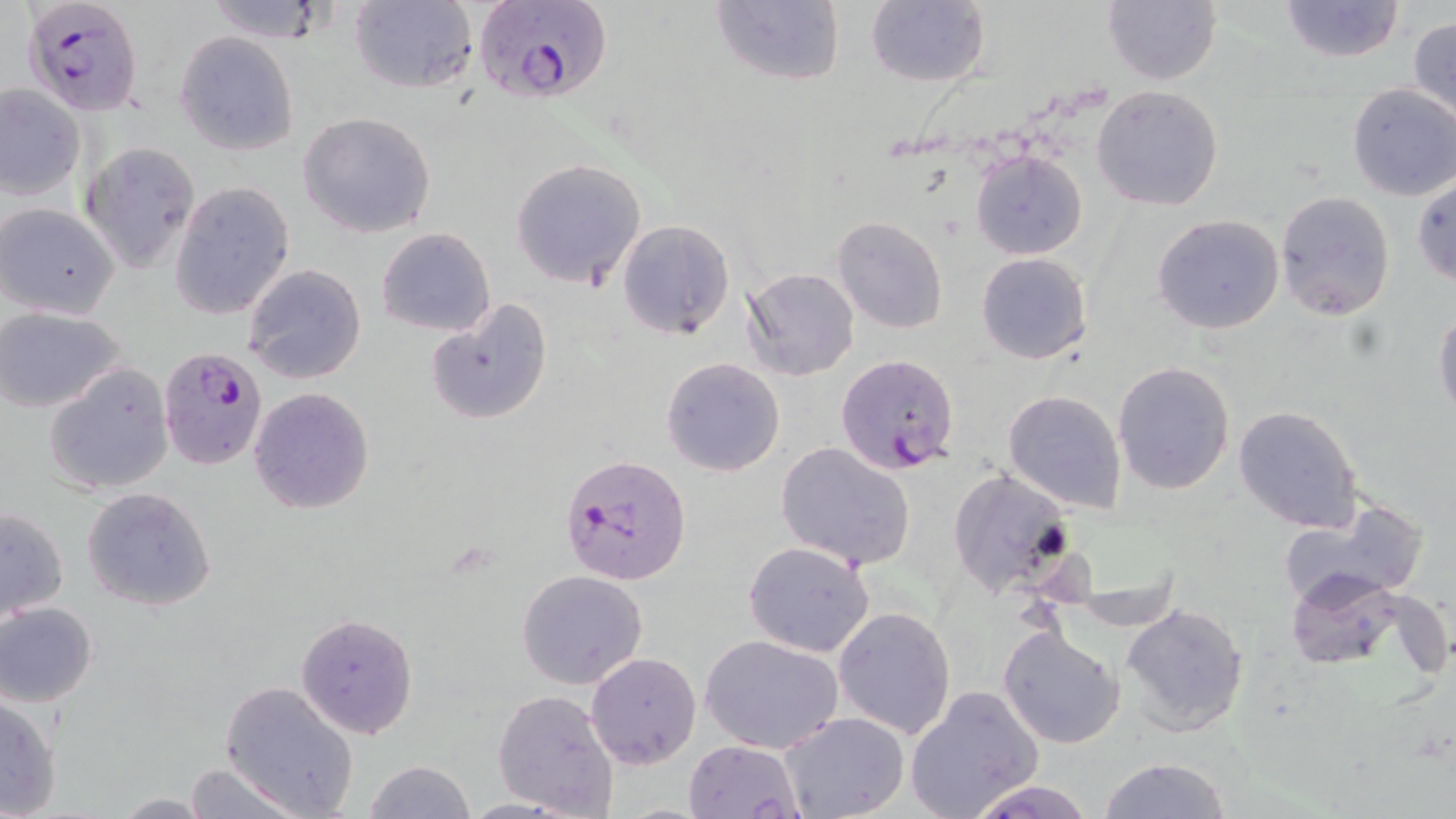

Summary:
  - Coordinate format: approximate bounding boxes as named x1/y1/x2/y2 corners in pixels
  - Plasmodium falciparum-infected red blood cell locations: (x1=471, y1=0, x2=612, y2=105), (x1=27, y1=1, x2=148, y2=119), (x1=158, y1=345, x2=269, y2=470), (x1=836, y1=353, x2=960, y2=474), (x1=562, y1=454, x2=691, y2=584)
  - Uninfected red blood cell locations: (x1=200, y1=0, x2=336, y2=43), (x1=347, y1=0, x2=478, y2=92), (x1=710, y1=0, x2=844, y2=87), (x1=1103, y1=0, x2=1221, y2=86), (x1=1280, y1=0, x2=1405, y2=63), (x1=866, y1=1, x2=989, y2=88), (x1=1408, y1=16, x2=1456, y2=124), (x1=175, y1=31, x2=299, y2=156), (x1=1346, y1=83, x2=1456, y2=201), (x1=1, y1=85, x2=86, y2=199), (x1=1091, y1=85, x2=1225, y2=211), (x1=298, y1=111, x2=437, y2=237), (x1=79, y1=142, x2=199, y2=273), (x1=970, y1=148, x2=1087, y2=261), (x1=510, y1=157, x2=648, y2=290), (x1=1412, y1=174, x2=1456, y2=288), (x1=169, y1=182, x2=294, y2=321), (x1=1274, y1=191, x2=1395, y2=322), (x1=1, y1=203, x2=121, y2=320), (x1=1153, y1=213, x2=1285, y2=335), (x1=831, y1=216, x2=948, y2=334), (x1=617, y1=219, x2=734, y2=340), (x1=375, y1=227, x2=496, y2=337), (x1=976, y1=253, x2=1091, y2=364), (x1=244, y1=264, x2=366, y2=385), (x1=741, y1=267, x2=859, y2=381), (x1=427, y1=297, x2=551, y2=425), (x1=0, y1=307, x2=127, y2=414), (x1=1432, y1=308, x2=1456, y2=421), (x1=660, y1=357, x2=786, y2=477), (x1=1113, y1=360, x2=1235, y2=495), (x1=44, y1=362, x2=174, y2=495), (x1=249, y1=386, x2=375, y2=514), (x1=1003, y1=389, x2=1127, y2=513), (x1=1233, y1=406, x2=1364, y2=533), (x1=775, y1=442, x2=916, y2=570), (x1=947, y1=469, x2=1075, y2=600), (x1=81, y1=486, x2=218, y2=611), (x1=1276, y1=500, x2=1430, y2=607), (x1=0, y1=507, x2=69, y2=620), (x1=743, y1=540, x2=876, y2=657), (x1=731, y1=563, x2=907, y2=720), (x1=516, y1=568, x2=648, y2=690), (x1=1286, y1=569, x2=1405, y2=672), (x1=1, y1=602, x2=98, y2=707), (x1=1120, y1=603, x2=1250, y2=739), (x1=833, y1=606, x2=958, y2=739), (x1=295, y1=612, x2=418, y2=738), (x1=998, y1=627, x2=1125, y2=749), (x1=700, y1=635, x2=844, y2=753), (x1=586, y1=652, x2=700, y2=768), (x1=219, y1=680, x2=360, y2=818), (x1=904, y1=684, x2=1046, y2=819), (x1=491, y1=687, x2=619, y2=816), (x1=1, y1=695, x2=61, y2=818), (x1=780, y1=712, x2=909, y2=819), (x1=684, y1=737, x2=803, y2=819), (x1=1099, y1=757, x2=1231, y2=819), (x1=364, y1=759, x2=475, y2=818), (x1=182, y1=762, x2=303, y2=819), (x1=965, y1=779, x2=1100, y2=819), (x1=112, y1=795, x2=215, y2=818)
  - Slide-level diagnosis: Plasmodium falciparum
  - Image size: 1456×819 pixels
  - Magnification: 1000x
  - Preparation: thin blood smear
  - Stain: May-Grünwald-Giemsa
  - Modality: light microscopy
  - Field of view: one of a larger specimen